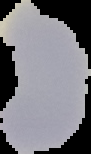

preparation = thin blood smear
image type = segmented cell region on a black background
image size = 91×154 pixels
malaria status = parasitized